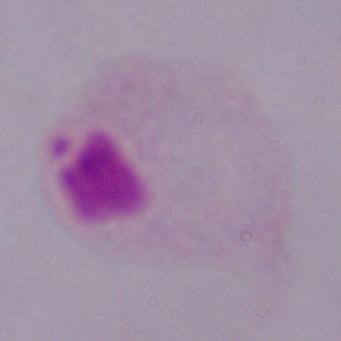 Photomicrograph. 1000x magnification. A trichomonad is shown.